Classify this cell by malaria status.
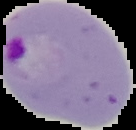
Parasitized.

Image is 136×130 pixels. The area outside the segmented cell region is set to black. From a thin blood smear.